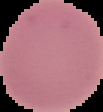

Summary:
  - Image size: 103×112 pixels
  - Image type: segmented cell region on a black background
  - Preparation: thin blood film
  - Malaria status: uninfected